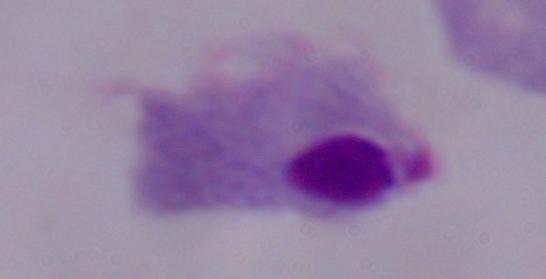

{
  "modality": "micrograph",
  "magnification": "1000x",
  "identification": "trichomonad"
}